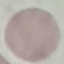

Summary:
  - Malaria status: uninfected
  - Preparation: thin blood film
  - Capture: smartphone through the microscope eyepiece
  - Stain: Giemsa
  - Image type: automatically extracted cell patch, resized to 64 × 64 pixels